Report the malaria status of this cell.
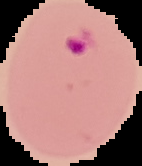

Parasitized.

Summary:
  - Image size: 142×166 pixels
  - Preparation: thin blood smear
  - Image type: segmented cell region on a black background